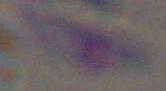
Summary:
  - Magnification: 1000x
  - Identification: Toxoplasma gondii
  - Modality: micrograph